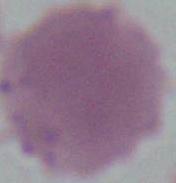
{
  "identification": "red blood cell",
  "modality": "photomicrograph",
  "magnification": "1000x"
}